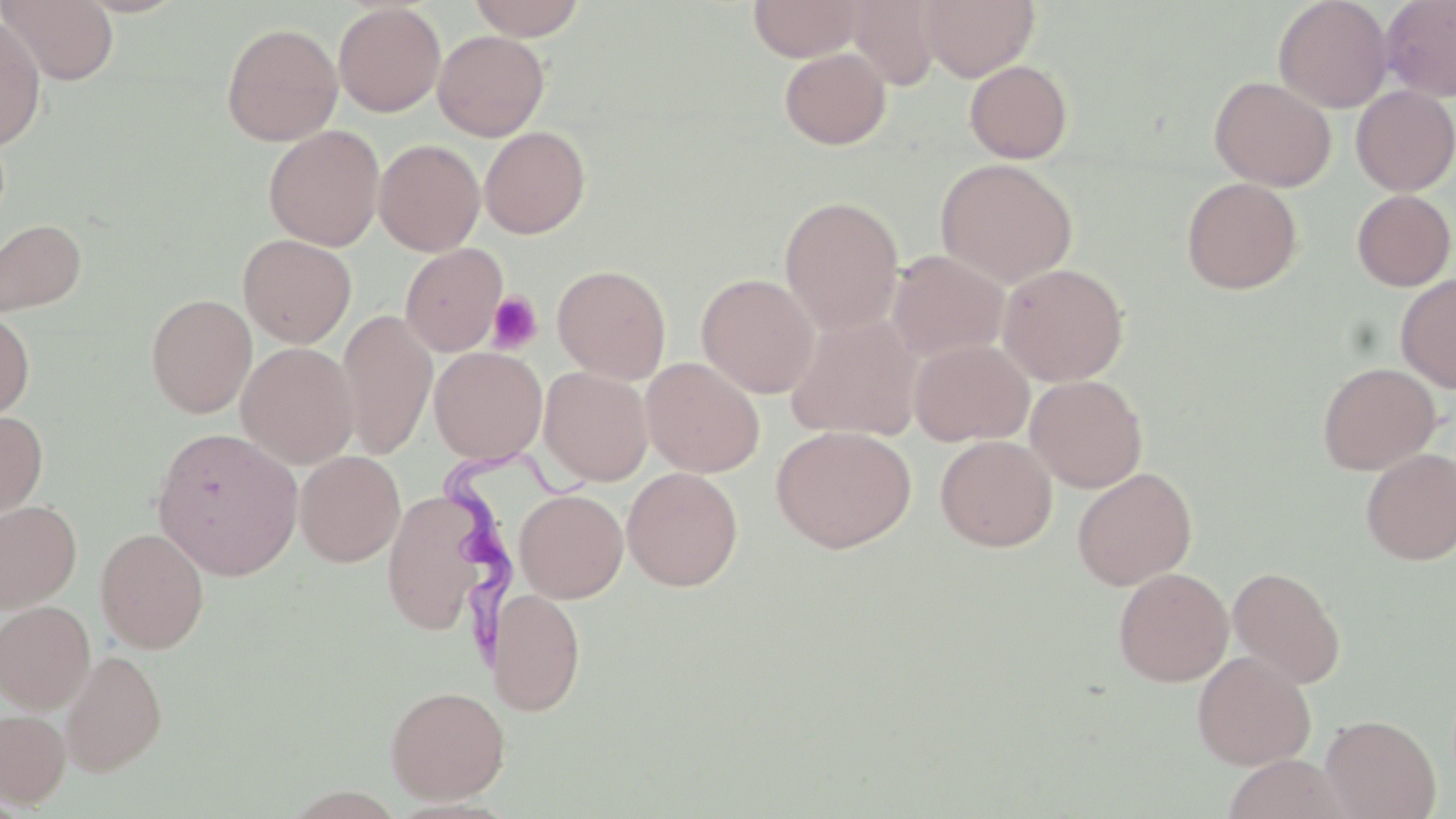

Summary:
  - Coordinate format: approximate bounding boxes as (x1,y1)-(x2,y2) corner pairs in pixels
  - Uninfected red blood cell locations: (466,0)-(588,40), (748,0)-(866,61), (917,0)-(1040,81), (1273,0)-(1393,112), (1380,0)-(1456,102), (2,1)-(119,85), (845,1)-(943,91), (333,3)-(446,117), (0,14)-(47,151), (221,22)-(342,146), (433,30)-(549,141), (779,47)-(891,149), (964,60)-(1073,163), (1209,75)-(1336,191), (1351,85)-(1456,195), (263,124)-(385,251), (479,126)-(590,239), (374,139)-(485,256), (935,158)-(1077,287), (1181,177)-(1303,294), (1352,189)-(1455,291), (779,196)-(904,334), (0,217)-(87,317), (809,219)-(968,350), (238,234)-(357,347), (400,243)-(508,356), (887,250)-(1009,362), (997,263)-(1129,385), (552,264)-(671,383), (697,273)-(820,398), (1395,273)-(1456,393), (146,294)-(256,417), (0,308)-(35,422), (338,309)-(437,458), (785,313)-(924,441), (909,339)-(1034,446), (236,342)-(359,469), (429,347)-(547,464), (642,357)-(765,477), (1317,362)-(1440,475), (539,367)-(653,486), (1025,374)-(1148,493), (0,410)-(48,522), (771,424)-(917,553), (151,427)-(303,580), (935,435)-(1057,552), (1360,448)-(1456,565), (295,450)-(405,566), (622,467)-(743,591), (1072,467)-(1197,590), (382,488)-(492,637), (514,489)-(628,603), (0,500)-(82,611), (95,527)-(210,653), (1227,566)-(1345,689), (1113,567)-(1233,687), (488,588)-(585,716), (0,600)-(95,713), (61,649)-(168,775), (1192,651)-(1315,770), (385,684)-(510,804), (0,709)-(70,808), (1320,714)-(1440,819), (1221,754)-(1351,819)
  - Trypanosoma brucei locations: (433,444)-(594,656)
  - Platelet locations: (485,291)-(543,354)
  - Slide-level diagnosis: Trypanosoma brucei
  - Magnification: 1000x
  - Preparation: thin blood film
  - Stain: May-Grünwald-Giemsa
  - Image size: 1456×819 pixels
  - Modality: optical microscopy
  - Field of view: one of a larger specimen